Identify the blood parasite species.
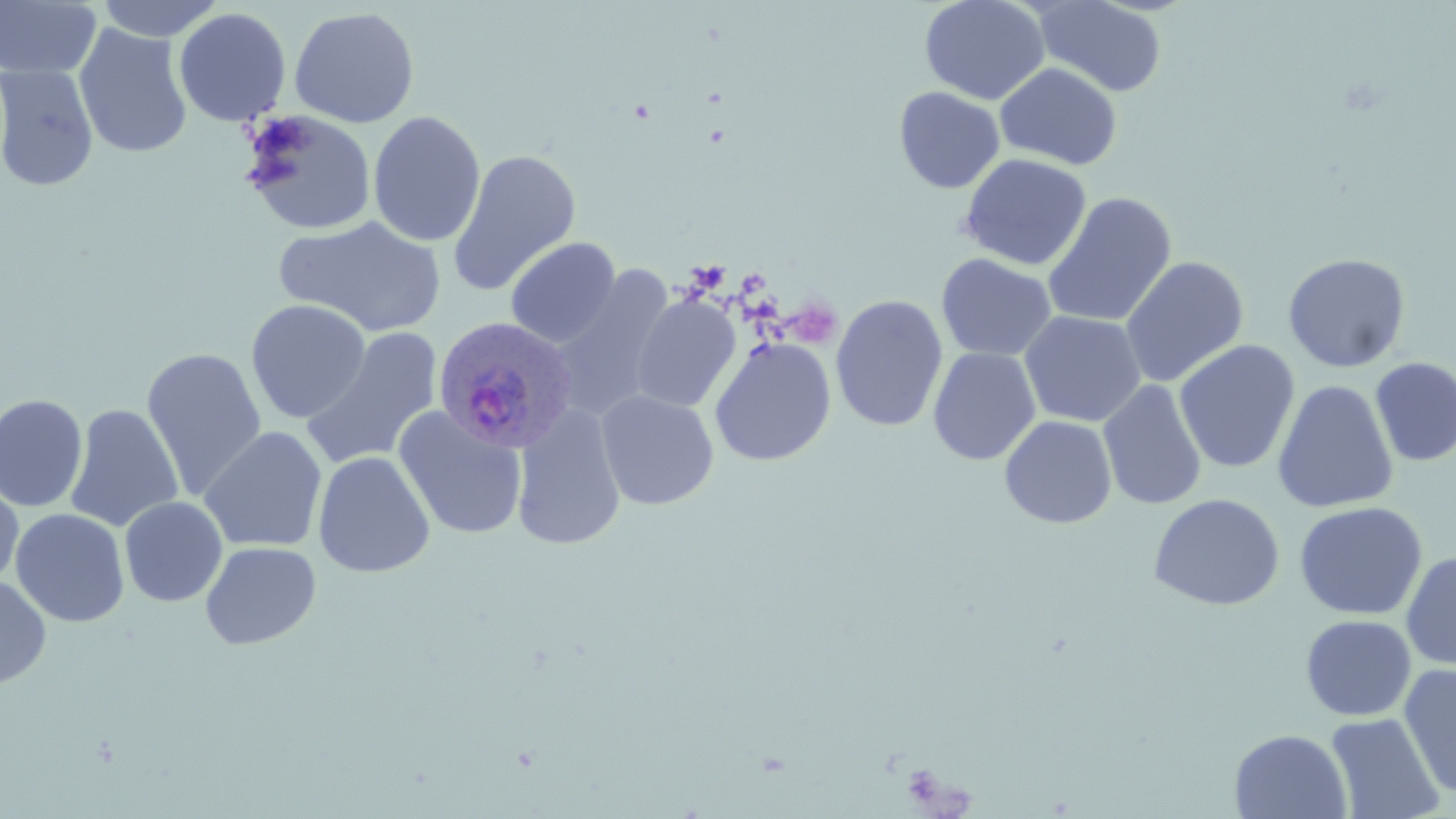

Plasmodium ovale.

Summary:
  - Coordinate format: approximate bounding boxes as [x1, y1, x2, y2] in pixels
  - Uninfected red blood cell locations: [0, 0, 102, 81], [93, 0, 226, 42], [919, 0, 1050, 105], [1033, 1, 1167, 97], [289, 6, 420, 128], [173, 7, 292, 127], [74, 24, 193, 158], [994, 62, 1123, 170], [0, 63, 99, 193], [893, 86, 1005, 194], [238, 109, 378, 236], [368, 110, 486, 248], [447, 148, 581, 297], [959, 153, 1092, 270], [1042, 192, 1177, 327], [275, 215, 445, 337], [505, 236, 621, 348], [936, 253, 1057, 362], [1282, 253, 1411, 373], [1120, 256, 1249, 387], [549, 265, 676, 421], [631, 295, 741, 413], [830, 295, 948, 432], [246, 298, 371, 424], [1018, 310, 1147, 427], [301, 326, 444, 471], [709, 337, 836, 467], [1174, 341, 1300, 474], [141, 346, 267, 501], [927, 347, 1041, 466], [1370, 356, 1456, 467], [1098, 379, 1207, 511], [1272, 379, 1398, 514], [596, 390, 719, 510], [0, 393, 88, 513], [65, 404, 183, 532], [510, 404, 626, 552], [392, 406, 528, 540], [999, 415, 1117, 529], [199, 426, 328, 553], [313, 451, 435, 577], [0, 476, 24, 592], [1148, 493, 1285, 611], [119, 496, 228, 607], [1293, 501, 1428, 621], [10, 508, 130, 627], [200, 541, 321, 650], [1401, 551, 1456, 671], [0, 575, 52, 691], [1300, 615, 1417, 721], [1398, 664, 1456, 800], [1325, 712, 1445, 819], [1229, 728, 1352, 819]
  - Plasmodium ovale-infected red blood cell locations: [431, 316, 576, 455]
  - Image size: 1456×819 pixels
  - Field of view: one of a larger specimen
  - Modality: optical microscopy
  - Preparation: thin blood smear
  - Stain: May-Grünwald-Giemsa
  - Magnification: 1000x